State which parasite is depicted.
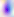

Toxoplasma gondii.

Summary:
  - Magnification: 400x
  - Modality: micrograph